Name the cell type shown.
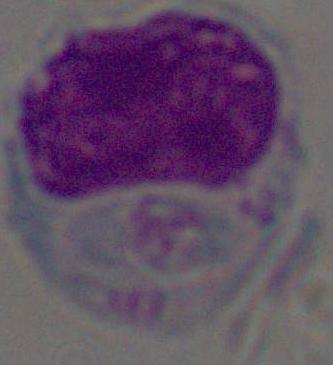

This is a leukocyte.

Captured at 1000x magnification. Micrograph.